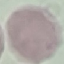

Result: no malaria parasites seen. Automatically extracted cell patch, resized to 64 × 64 pixels. Thin blood film. Giemsa-stained preparation. Photographed with a smartphone camera at the microscope eyepiece.